Assess this cell for malaria.
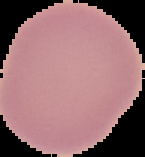
Uninfected.

Summary:
  - Image type: segmented cell region on a black background
  - Image size: 145×157 pixels
  - Preparation: thin blood film